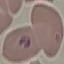

Result: malaria parasites identified. Photographed with a smartphone camera at the microscope eyepiece. Thin smear of blood. Giemsa stain. Cell patch, automatically extracted from a larger field of view and resized to 64 × 64 pixels.